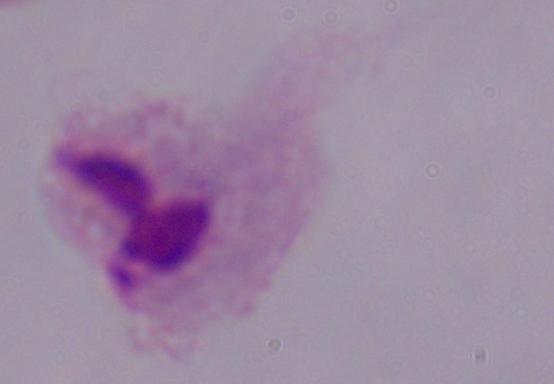

Captured at 1000x magnification. A trichomonad is seen. Photomicrograph.